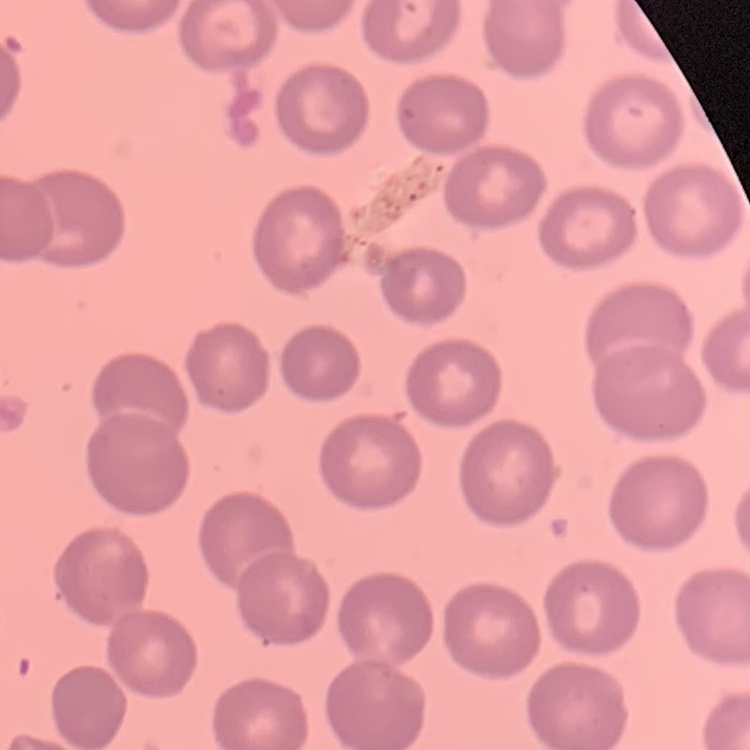
erythrocyte morphology = no rouleaux formation
stain = Field's or Giemsa
image type = one tile cut from a larger photomicrograph
preparation = thin blood film